Assess this cell for malaria.
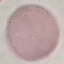

Uninfected.

{
  "image_type": "automatically extracted cell patch, resized to 64 × 64 pixels",
  "stain": "Giemsa",
  "capture": "smartphone through the microscope eyepiece",
  "preparation": "thin blood smear"
}